Give the position of every Plasmodium falciparum parasite, noting its life-cycle stage.
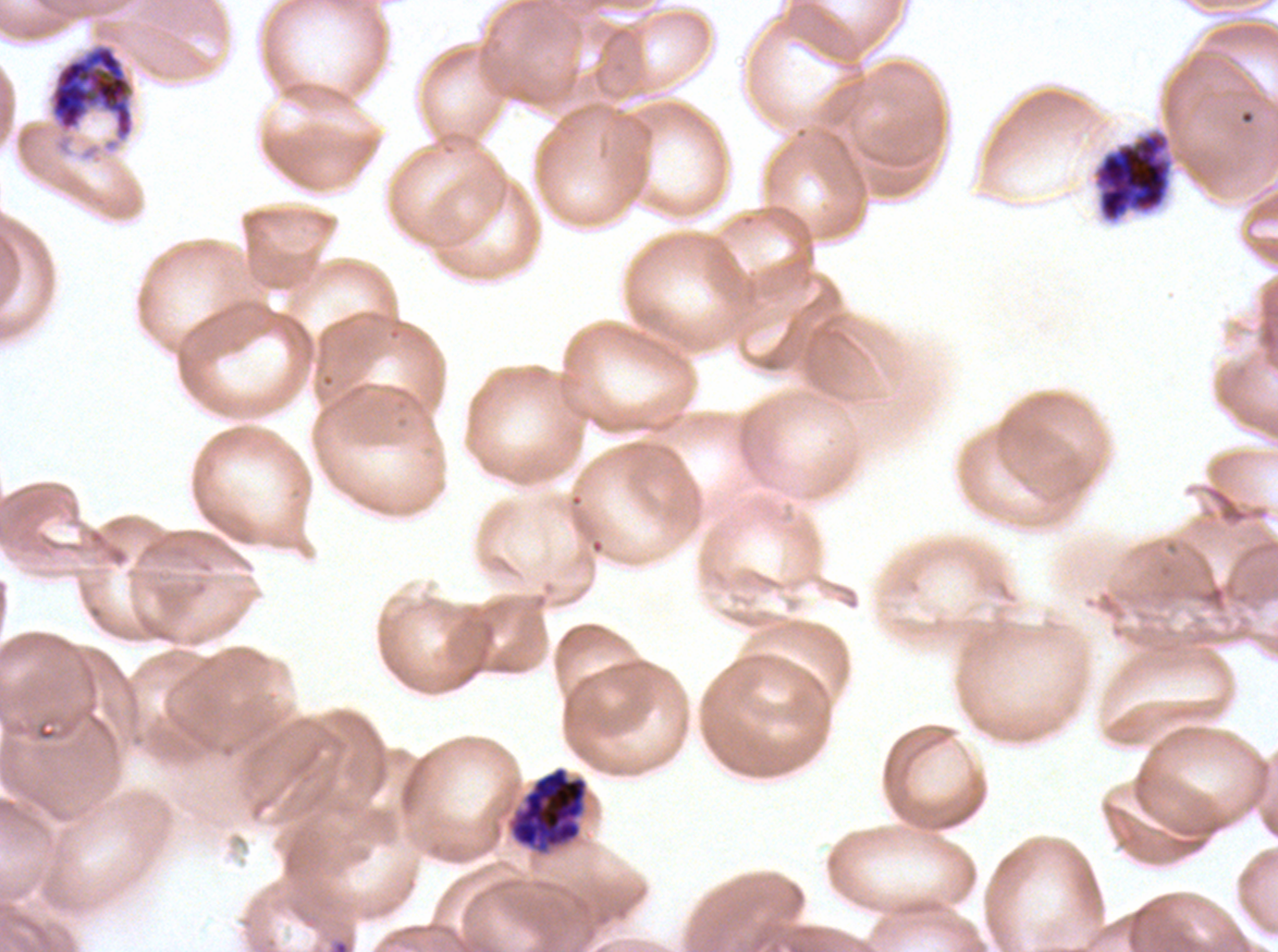
Approximate bounding boxes as {x1, y1, x2, y2} in pixels.
Rings: {327, 937, 351, 951}.
Early schizonts: {51, 45, 132, 137}.
Late schizonts: {1094, 130, 1173, 222}, {510, 766, 587, 848}.
No late-ring/early-trophozoite forms, mid trophozoites, late trophozoites, segmenters, or gametocytes observed.

Summary:
  - Image size: 1278×952 pixels
  - Preparation: thin blood film
  - Specimen: ex-vivo Plasmodium falciparum culture from a patient in The Gambia, grown for 24 to 48 hours
  - Stain: Giemsa
  - Life-cycle stages observed: ring, early schizont, late schizont
  - Field of view: one sub-image of a larger composite